Name the parasite shown.
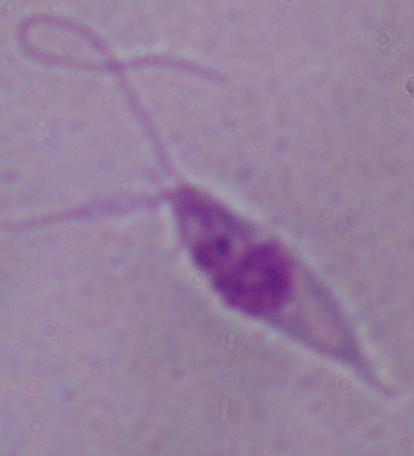
This is Leishmania.

Micrograph. Captured at 1000x magnification.